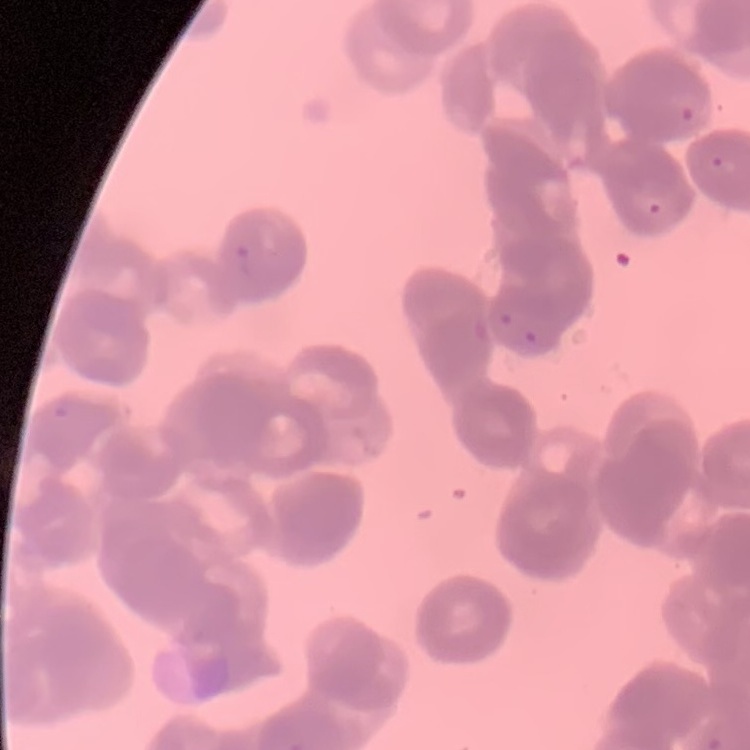

The red blood cells exhibit rouleaux formation. Stained with either Field's or Giemsa. Thin peripheral smear. Square crop of a larger photomicrograph.